Report the malaria status of this cell.
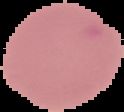
Uninfected.

Summary:
  - Image type: cell region segmented out of the field of view; surrounding area masked to black
  - Image size: 124×112 pixels
  - Preparation: thin blood film